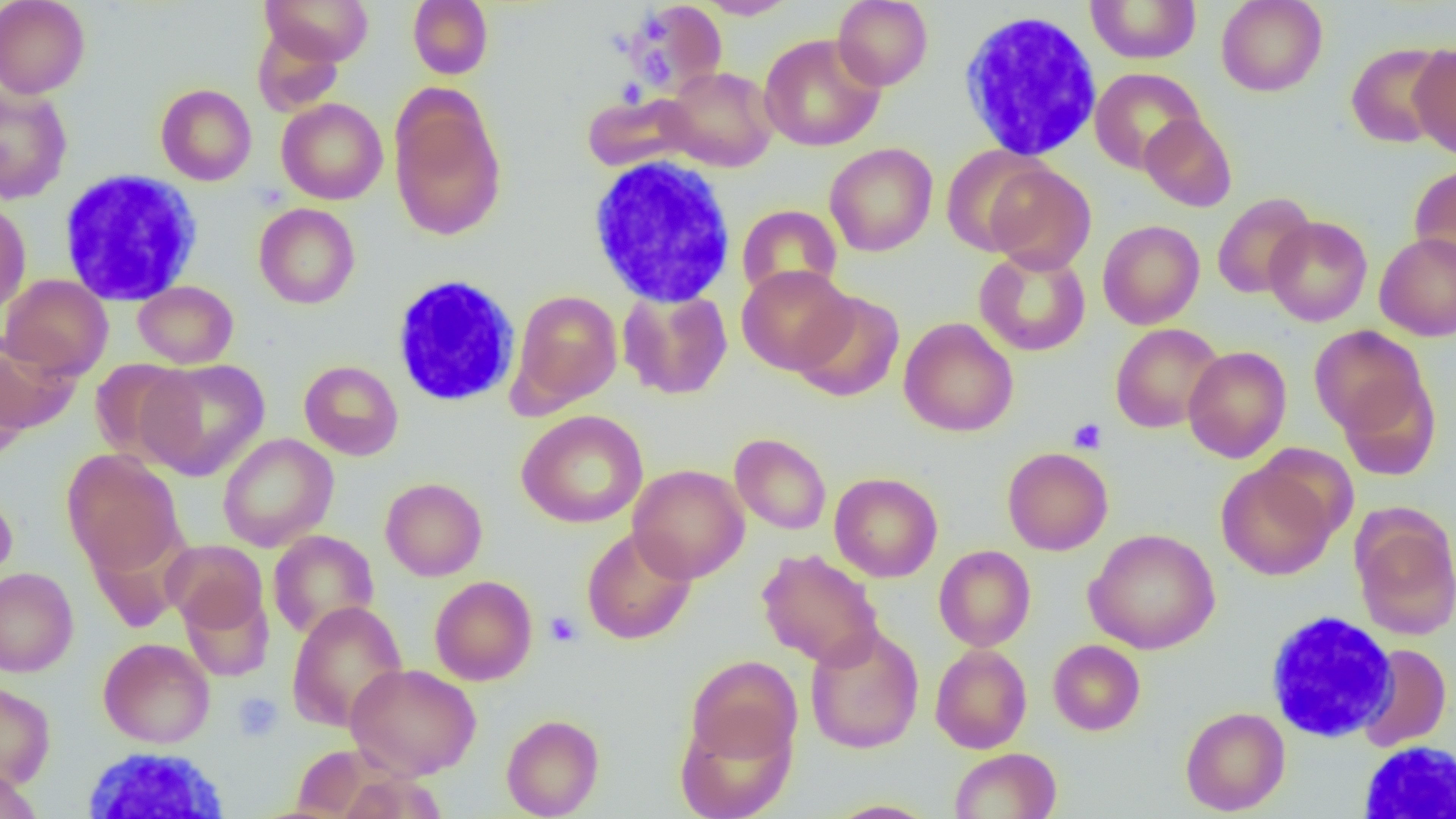
slide-level diagnosis = no evidence of blood parasites
modality = optical microscopy
magnification = 1000x
field of view = single
uninfected red blood cell locations = approximate bounding boxes as [x1, y1, x2, y2] in pixels: [0, 0, 90, 99], [260, 0, 374, 65], [407, 0, 493, 79], [833, 0, 933, 90], [1085, 0, 1202, 64], [1216, 0, 1327, 97], [624, 1, 727, 98], [696, 1, 799, 19], [252, 26, 344, 115], [759, 33, 886, 152], [1345, 42, 1451, 148], [1409, 42, 1456, 160], [661, 66, 778, 172], [1089, 68, 1205, 174], [155, 83, 257, 185], [0, 87, 72, 203], [389, 92, 507, 242], [582, 92, 701, 173], [276, 98, 388, 205], [1139, 113, 1237, 212], [824, 143, 938, 257], [941, 144, 1054, 257], [983, 162, 1096, 274], [1409, 163, 1456, 273], [1212, 192, 1316, 300], [0, 198, 32, 315], [254, 203, 360, 309], [737, 204, 842, 302], [1263, 216, 1373, 326], [1098, 220, 1205, 329], [1375, 232, 1456, 342], [974, 248, 1091, 356], [736, 264, 855, 374], [1, 274, 114, 380], [133, 280, 238, 368], [617, 288, 733, 400], [511, 289, 622, 409], [791, 290, 905, 403], [898, 317, 1018, 437], [1110, 323, 1224, 433], [1309, 325, 1429, 436], [0, 337, 79, 435], [1183, 345, 1292, 463], [89, 358, 198, 466], [139, 359, 270, 481], [299, 360, 403, 460], [0, 361, 29, 462], [1337, 373, 1442, 482], [516, 410, 648, 528], [217, 433, 338, 552], [730, 433, 832, 535], [1002, 447, 1113, 555], [62, 449, 185, 576], [1216, 458, 1340, 581], [628, 463, 750, 583], [829, 472, 943, 582], [380, 477, 487, 581], [0, 489, 17, 588], [1352, 513, 1456, 640], [581, 526, 697, 644], [1084, 528, 1220, 654], [268, 530, 379, 639], [162, 540, 268, 635], [933, 545, 1036, 651], [757, 548, 883, 669], [0, 567, 79, 677], [429, 576, 537, 685], [179, 584, 275, 680], [287, 601, 408, 732], [805, 625, 924, 754], [98, 637, 215, 748], [1048, 639, 1145, 735], [1357, 643, 1451, 752], [930, 644, 1032, 753], [685, 655, 801, 767], [345, 662, 481, 778], [0, 679, 56, 790], [1180, 707, 1290, 815], [675, 709, 796, 819], [501, 714, 604, 819], [949, 747, 1062, 819], [0, 765, 42, 819], [826, 800, 939, 818]
image size = 1456×819 pixels
preparation = thin blood film
platelet locations = approximate bounding boxes as [x1, y1, x2, y2] in pixels: [1068, 418, 1107, 454], [544, 611, 582, 647], [232, 692, 283, 741]
white blood cell locations = approximate bounding boxes as [x1, y1, x2, y2] in pixels: [957, 12, 1103, 162], [586, 153, 738, 306], [57, 170, 203, 307], [389, 274, 521, 408], [1265, 609, 1398, 743], [1358, 740, 1456, 818], [78, 746, 234, 817]